State which cell type is depicted.
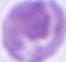
An erythrocyte.

Photomicrograph. Captured at 1000x magnification.